Classify this cell by malaria status.
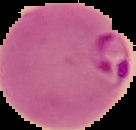

Parasitized.

image size = 136×130 pixels
preparation = thin blood film
image type = segmented cell region on a black background